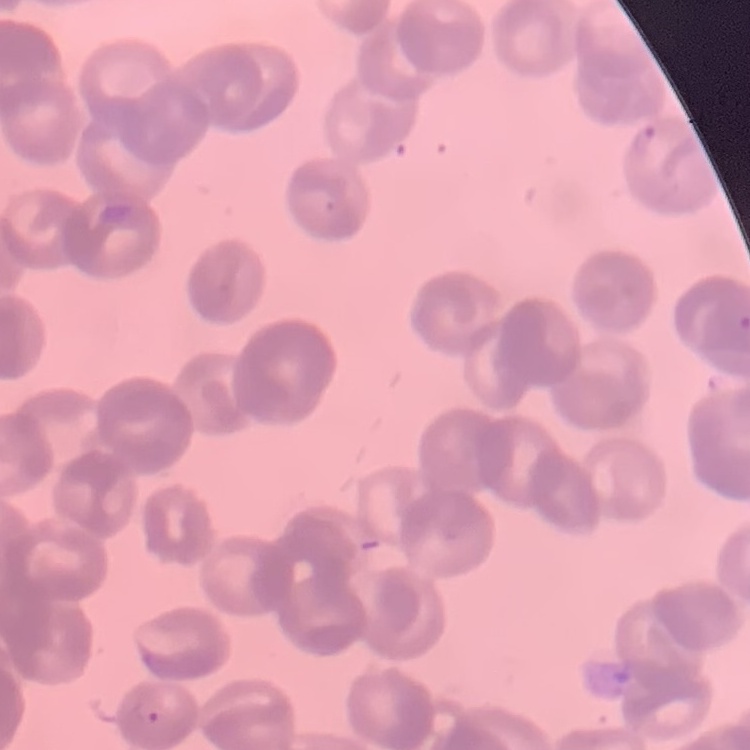
Summary:
  - Red blood cell morphology: rouleaux formation
  - Preparation: thin peripheral smear
  - Image type: one tile cut from a larger photomicrograph
  - Stain: Field's or Giemsa